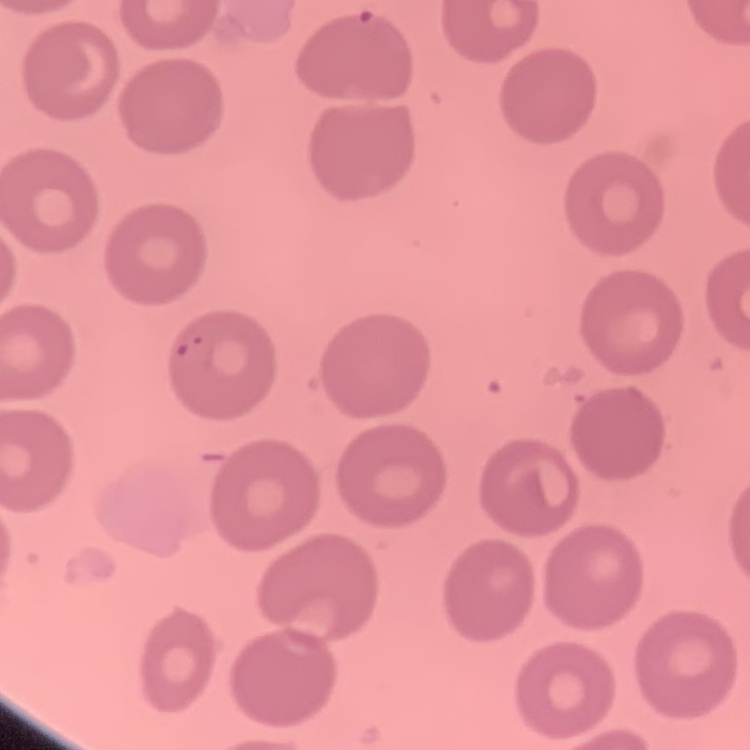

Summary:
  - Erythrocyte morphology: no rouleaux formation
  - Image type: one tile cut from a larger photomicrograph
  - Stain: Field's or Giemsa
  - Preparation: thin blood smear